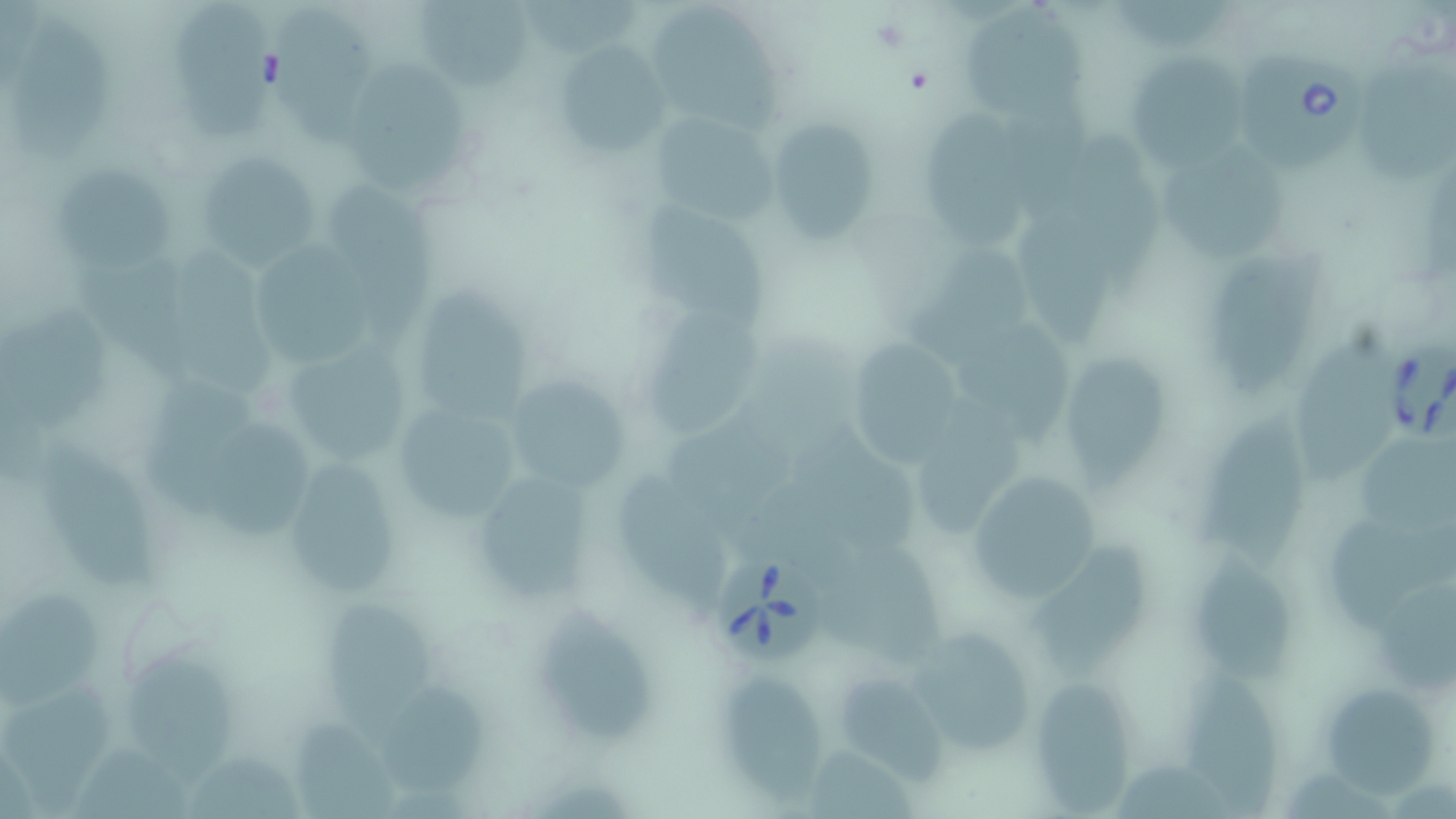
Approximate bounding boxes as named x1/y1/x2/y2 corners in pixels. Uninfected red blood cell locations: (x1=170, y1=0, x2=268, y2=139), (x1=522, y1=0, x2=644, y2=55), (x1=1114, y1=0, x2=1239, y2=53), (x1=413, y1=1, x2=535, y2=93), (x1=270, y1=5, x2=379, y2=147), (x1=961, y1=5, x2=1089, y2=120), (x1=646, y1=10, x2=785, y2=133), (x1=9, y1=14, x2=119, y2=166), (x1=551, y1=41, x2=668, y2=158), (x1=1129, y1=50, x2=1254, y2=176), (x1=347, y1=59, x2=462, y2=198), (x1=1358, y1=65, x2=1456, y2=183), (x1=916, y1=93, x2=1031, y2=254), (x1=1006, y1=104, x2=1089, y2=220), (x1=649, y1=107, x2=779, y2=227), (x1=765, y1=119, x2=880, y2=244), (x1=1078, y1=132, x2=1170, y2=295), (x1=1155, y1=141, x2=1295, y2=264), (x1=194, y1=150, x2=327, y2=270), (x1=57, y1=160, x2=180, y2=276), (x1=330, y1=182, x2=440, y2=352), (x1=628, y1=193, x2=781, y2=337), (x1=1018, y1=205, x2=1116, y2=342), (x1=1208, y1=236, x2=1326, y2=393), (x1=170, y1=243, x2=281, y2=399), (x1=251, y1=247, x2=382, y2=366), (x1=906, y1=249, x2=1032, y2=363), (x1=410, y1=286, x2=538, y2=424), (x1=0, y1=308, x2=117, y2=426), (x1=641, y1=309, x2=761, y2=436), (x1=964, y1=324, x2=1069, y2=451), (x1=1289, y1=328, x2=1402, y2=485), (x1=842, y1=337, x2=967, y2=465), (x1=289, y1=346, x2=415, y2=468), (x1=1061, y1=353, x2=1175, y2=487), (x1=503, y1=374, x2=634, y2=494), (x1=916, y1=395, x2=1027, y2=530), (x1=390, y1=396, x2=528, y2=525), (x1=1200, y1=401, x2=1307, y2=573), (x1=202, y1=417, x2=329, y2=537), (x1=668, y1=422, x2=794, y2=528), (x1=803, y1=427, x2=924, y2=557), (x1=38, y1=431, x2=162, y2=591), (x1=1359, y1=439, x2=1456, y2=536), (x1=273, y1=458, x2=406, y2=599), (x1=615, y1=468, x2=728, y2=606), (x1=464, y1=469, x2=602, y2=607), (x1=956, y1=469, x2=1112, y2=608), (x1=740, y1=482, x2=854, y2=588), (x1=1322, y1=521, x2=1456, y2=632), (x1=1183, y1=546, x2=1299, y2=685), (x1=1028, y1=551, x2=1157, y2=683), (x1=833, y1=554, x2=949, y2=670), (x1=1375, y1=575, x2=1456, y2=685), (x1=2, y1=586, x2=103, y2=720), (x1=318, y1=592, x2=440, y2=747), (x1=538, y1=602, x2=663, y2=746), (x1=896, y1=631, x2=1042, y2=754), (x1=124, y1=653, x2=243, y2=792), (x1=1179, y1=660, x2=1279, y2=817), (x1=718, y1=670, x2=823, y2=803), (x1=833, y1=670, x2=963, y2=779), (x1=1319, y1=673, x2=1434, y2=799), (x1=380, y1=676, x2=490, y2=797), (x1=1035, y1=679, x2=1135, y2=813), (x1=5, y1=692, x2=120, y2=812), (x1=289, y1=713, x2=401, y2=819), (x1=806, y1=743, x2=919, y2=819), (x1=1116, y1=752, x2=1232, y2=817). Babesia divergens-infected red blood cell locations: (x1=1236, y1=49, x2=1373, y2=179), (x1=1396, y1=345, x2=1454, y2=445), (x1=714, y1=552, x2=827, y2=663). Slide-level diagnosis: Babesia divergens. Captured at 1000x magnification. Single field of view. Optical microscopy. Thin blood film. Image is 1456×819 pixels. May-Grünwald-Giemsa-stained preparation.